Locate every uninfected red blood cell.
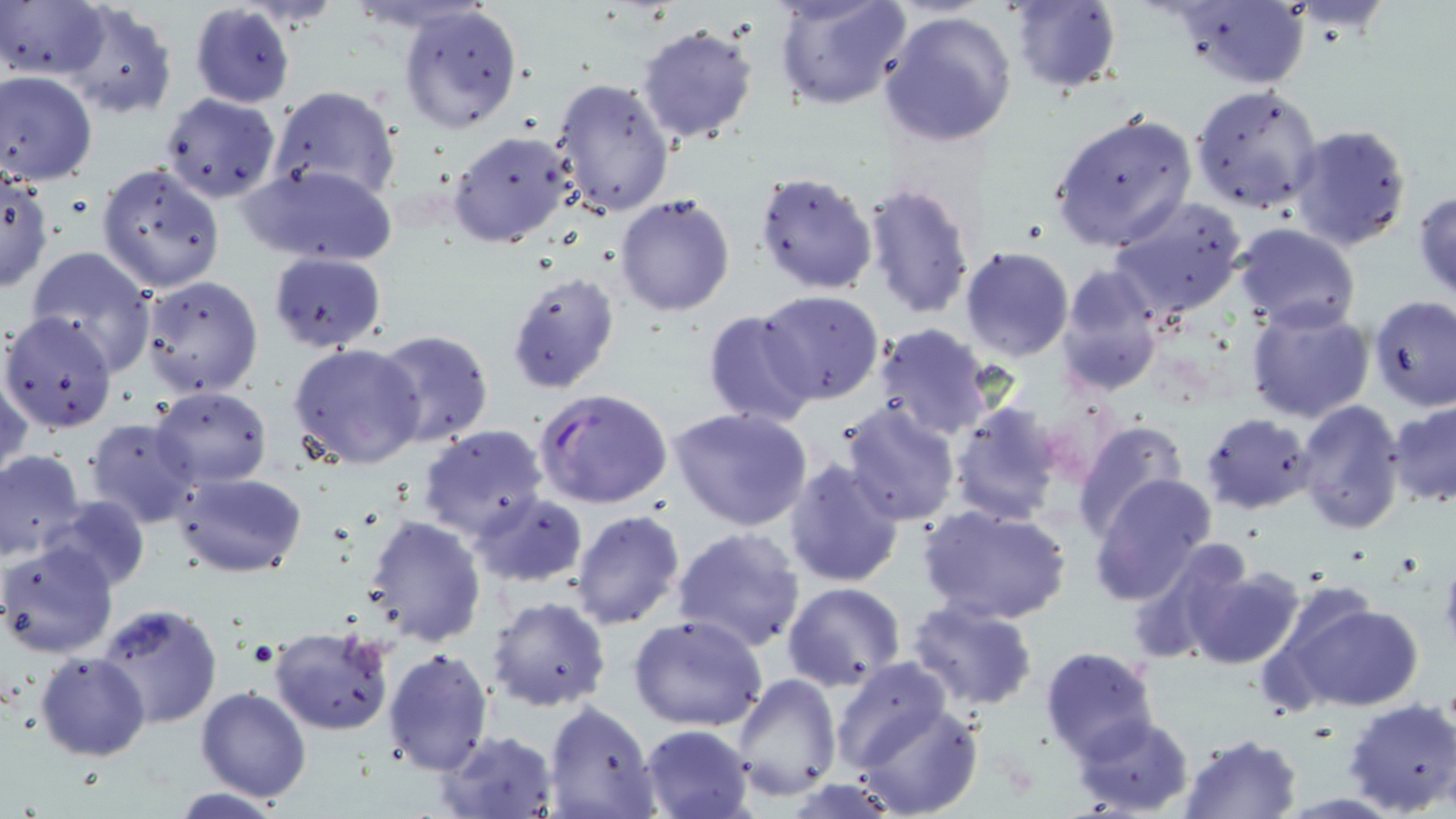

Approximate bounding boxes as (x1, y1, x2, y2) in pixels.
Uninfected red blood cells: (775, 0, 914, 111), (1006, 1, 1123, 93), (2, 2, 108, 83), (60, 2, 177, 120), (1173, 2, 1310, 90), (189, 4, 295, 109), (397, 5, 523, 134), (877, 10, 1017, 148), (636, 22, 761, 145), (0, 71, 98, 186), (551, 77, 676, 218), (1188, 85, 1325, 214), (271, 86, 401, 202), (160, 92, 281, 204), (1048, 110, 1199, 253), (1288, 121, 1415, 251), (447, 131, 576, 249), (241, 162, 398, 266), (97, 163, 224, 292), (754, 170, 878, 295), (0, 172, 51, 292), (859, 181, 977, 321), (1413, 188, 1456, 303), (615, 193, 737, 316), (1106, 196, 1250, 321), (1233, 223, 1361, 331), (24, 244, 158, 372), (958, 246, 1073, 362), (269, 251, 389, 351), (1057, 265, 1166, 395), (505, 271, 621, 394), (138, 274, 265, 398), (757, 289, 888, 406), (1370, 295, 1455, 411), (1245, 303, 1375, 425), (702, 309, 820, 428), (1, 310, 120, 435), (871, 325, 996, 442), (371, 328, 494, 449), (288, 341, 426, 469), (0, 369, 32, 485), (151, 385, 272, 487), (1294, 398, 1408, 535), (1388, 399, 1456, 509), (840, 400, 960, 524), (949, 402, 1065, 522), (671, 408, 813, 533), (1201, 412, 1316, 514), (84, 417, 202, 531), (1072, 420, 1189, 539), (417, 424, 550, 542), (0, 449, 87, 561), (784, 459, 907, 589), (171, 471, 307, 576), (1090, 473, 1219, 603), (469, 491, 589, 588), (42, 495, 150, 594), (919, 503, 1070, 626), (571, 509, 686, 629), (362, 515, 487, 646), (671, 525, 806, 652), (1127, 537, 1261, 663), (1, 540, 119, 659), (1180, 560, 1306, 670), (782, 581, 908, 693), (1276, 593, 1425, 712), (488, 596, 611, 712), (907, 600, 1039, 711), (96, 602, 224, 730), (628, 613, 770, 732), (267, 626, 396, 737), (1040, 646, 1161, 761), (384, 647, 495, 776), (36, 652, 150, 761), (831, 657, 952, 774), (732, 673, 841, 800), (195, 687, 311, 802), (1342, 698, 1456, 816), (543, 700, 660, 819), (854, 701, 984, 818), (1070, 713, 1195, 818), (640, 724, 756, 819), (438, 730, 558, 819), (1179, 732, 1304, 819).

slide-level diagnosis = Plasmodium falciparum
magnification = 1000x
stain = May-Grünwald-Giemsa
modality = light microscopy
Plasmodium falciparum-infected red blood cell locations = approximate bounding boxes as (x1, y1, x2, y2) in pixels: (534, 388, 675, 511)
preparation = thin blood film
image size = 1456×819 pixels
field of view = one of a larger specimen